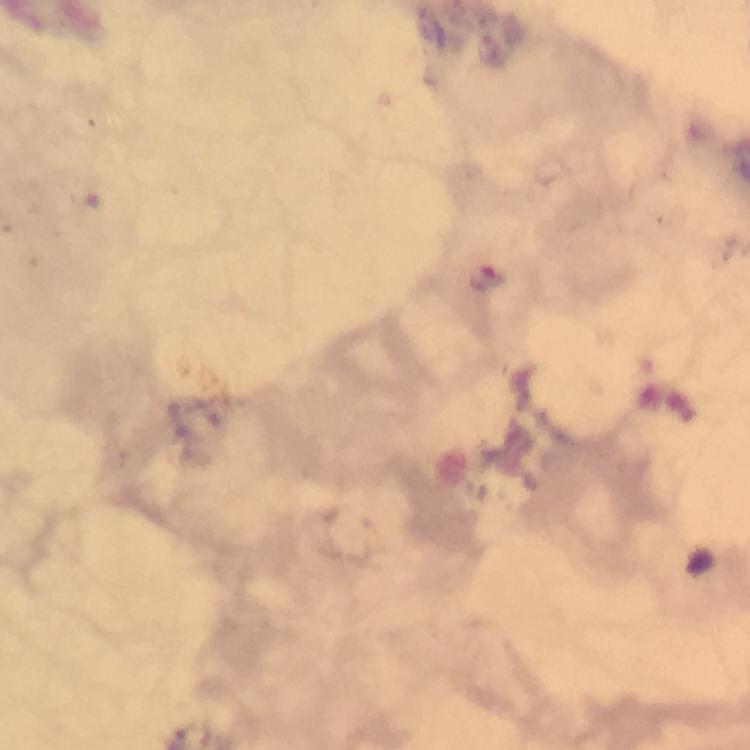

Approximate centers as [x, y] in pixels. Plasmodium parasite locations: [485, 279]. Image is 750×750 pixels. Thick blood smear. Immersion oil applied. Giemsa-stained preparation. Smartphone photograph taken through a microscope. Cropped region of a single field of view. At 100x magnification. From a diagnostic examination for malaria.